Classify this cell by malaria status.
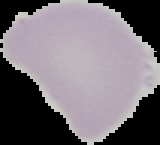
It is uninfected.

image size = 160×145 pixels
preparation = thin blood film
image type = segmented cell region on a black background